Classify this cell by malaria status.
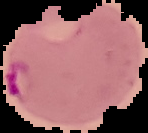

Parasitized.

{
  "preparation": "thin blood film",
  "image_size": "148×133 pixels",
  "image_type": "segmented cell region on a black background"
}